Mark where platelets are.
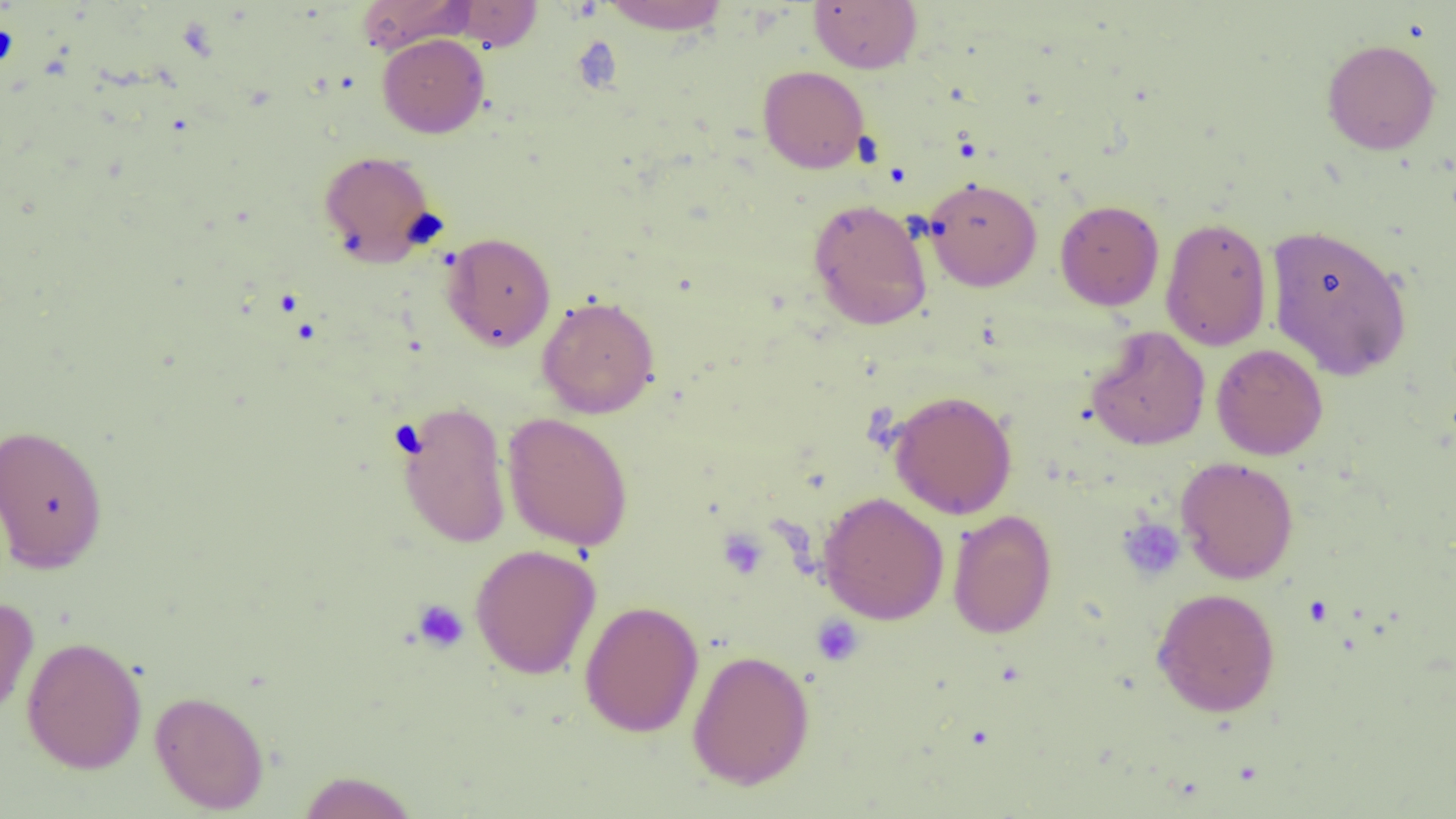
Approximate bounding boxes as (x1,y1)-(x2,y2) corner pairs in pixels.
Platelets: (1117,518)-(1185,581), (717,528)-(769,580), (412,599)-(469,653), (811,615)-(865,666).

Summary:
  - Uninfected red blood cell locations: (355,0)-(474,54), (598,0)-(731,34), (808,0)-(922,73), (445,1)-(544,51), (377,33)-(489,138), (1321,39)-(1440,155), (758,66)-(869,173), (318,150)-(438,266), (923,177)-(1042,291), (808,198)-(932,331), (1055,199)-(1164,310), (1160,217)-(1272,351), (1265,224)-(1413,381), (442,232)-(556,351), (537,295)-(660,419), (1086,326)-(1210,451), (1211,343)-(1328,460), (888,390)-(1018,519), (397,400)-(512,549), (502,412)-(633,551), (0,423)-(108,573), (1175,456)-(1299,584), (818,492)-(949,625), (947,509)-(1058,639), (469,543)-(601,680), (1151,587)-(1281,717), (0,594)-(39,725), (579,599)-(704,737), (21,636)-(147,774), (686,649)-(815,790), (149,689)-(269,814), (295,770)-(420,818)
  - Slide-level diagnosis: negative for blood parasites
  - Image size: 1456×819 pixels
  - Modality: optical microscopy
  - Magnification: 1000x
  - Preparation: thin blood film
  - Field of view: one of a larger specimen